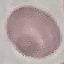

result = negative for malaria parasites
preparation = thin blood smear
image type = automatically extracted cell patch, resized to 64 × 64 pixels
capture = smartphone through the microscope eyepiece
stain = Giemsa